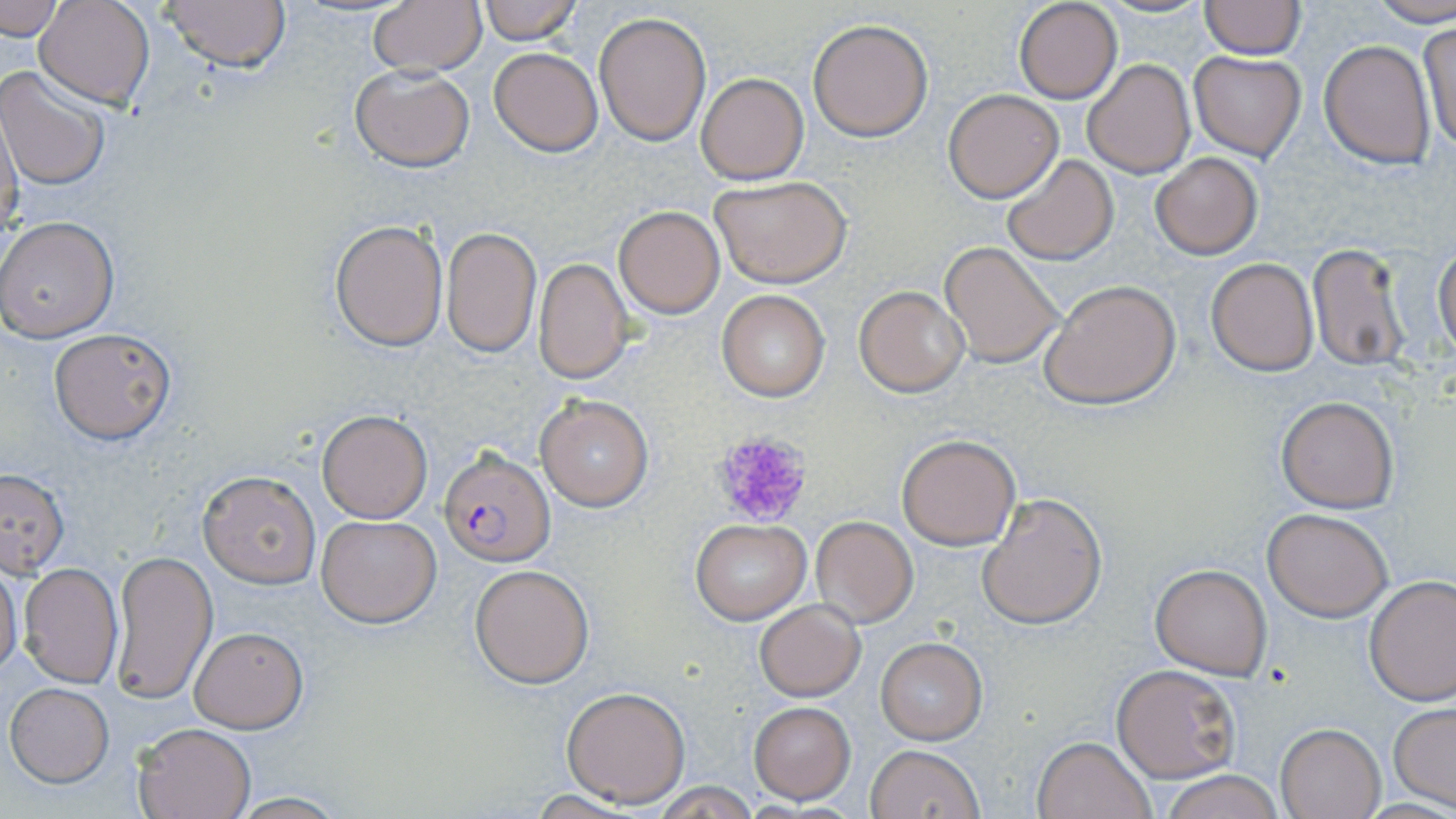 Approximate bounding boxes as (x1, y1, x2, y2) in pixels. Platelet locations: (709, 430, 815, 529). Plasmodium falciparum-infected red blood cell locations: (440, 446, 555, 565). Uninfected red blood cell locations: (34, 0, 155, 108), (160, 0, 292, 74), (367, 0, 486, 78), (475, 0, 583, 46), (1012, 0, 1122, 103), (1200, 0, 1305, 58), (0, 1, 66, 39), (1369, 1, 1456, 27), (593, 10, 711, 147), (807, 18, 933, 141), (1417, 22, 1456, 154), (1319, 40, 1436, 167), (490, 48, 602, 156), (1189, 50, 1306, 161), (1081, 59, 1195, 179), (348, 64, 475, 171), (0, 67, 112, 190), (697, 73, 807, 183), (943, 89, 1064, 202), (0, 105, 23, 241), (1149, 151, 1264, 258), (1001, 154, 1118, 266), (709, 176, 852, 288), (613, 207, 724, 318), (0, 216, 119, 341), (330, 218, 448, 351), (440, 226, 542, 360), (939, 241, 1066, 369), (1307, 241, 1412, 369), (1434, 244, 1455, 359), (534, 257, 634, 384), (1206, 258, 1319, 375), (1040, 278, 1182, 410), (854, 286, 969, 396), (716, 289, 830, 401), (48, 326, 178, 445), (535, 393, 654, 511), (1275, 394, 1400, 513), (316, 408, 433, 523), (895, 432, 1021, 551), (0, 468, 70, 579), (197, 469, 321, 588), (976, 492, 1108, 630), (1264, 507, 1393, 620), (316, 514, 441, 628), (809, 515, 916, 626), (690, 519, 812, 623), (111, 549, 217, 705), (0, 563, 24, 681), (18, 563, 123, 688), (1148, 563, 1272, 680), (469, 564, 595, 688), (1364, 575, 1456, 705), (754, 601, 865, 701), (188, 626, 307, 732), (876, 638, 986, 744), (1111, 664, 1239, 783), (5, 683, 114, 786), (560, 686, 692, 807), (749, 702, 855, 803), (1389, 702, 1456, 811), (131, 721, 256, 818), (1276, 723, 1386, 818), (1031, 735, 1157, 819), (865, 744, 983, 819), (1159, 769, 1286, 819), (651, 782, 759, 817), (520, 790, 647, 819), (223, 793, 352, 818). Slide-level diagnosis: Plasmodium falciparum. Single field of view. Image is 1456×819 pixels. May-Grünwald-Giemsa-stained preparation. Light microscopy. Thin blood smear. Captured at 1000x magnification.